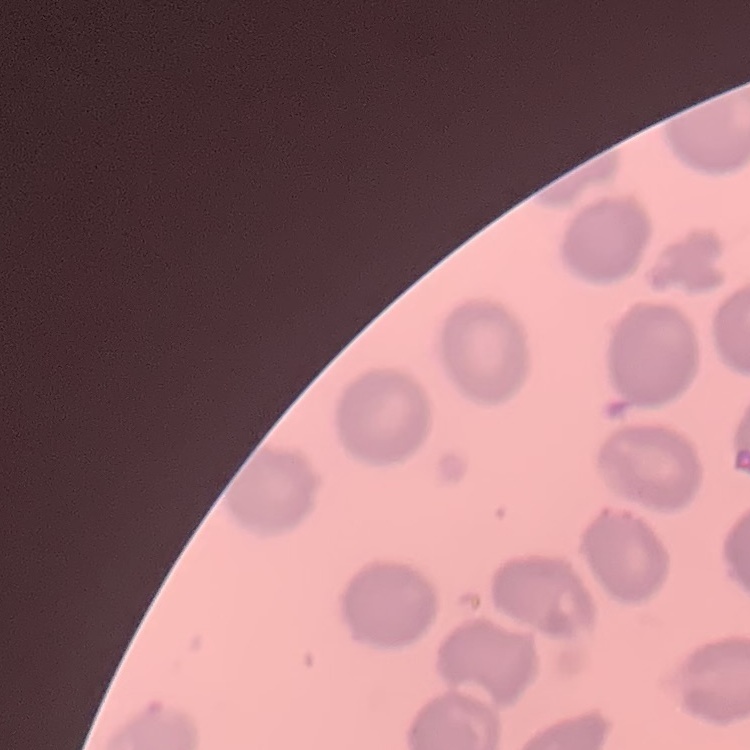

The red blood cells exhibit no rouleaux formation. Field's or Giemsa stain. Thin blood film. Square crop of a larger photomicrograph.